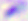

Summary:
  - Modality: micrograph
  - Identification: Toxoplasma gondii
  - Magnification: 400x